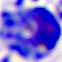

modality = micrograph
identification = white blood cell
magnification = 400x